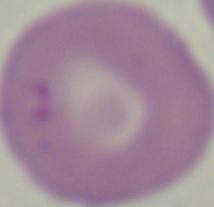
{
  "identification": "Babesia",
  "modality": "photomicrograph",
  "magnification": "1000x"
}